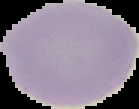 Result: negative for Plasmodium parasites. Cell region segmented out of the field of view; the surrounding area is masked to black. Image is 139×109 pixels. From a thin blood smear.